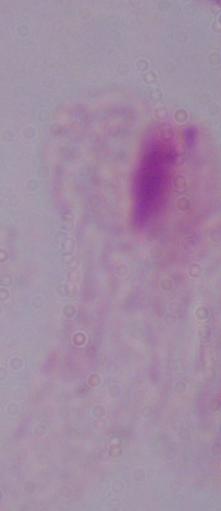
magnification = 1000x
modality = micrograph
identification = trichomonad